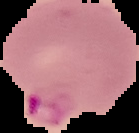

Summary:
  - Malaria status: parasitized
  - Preparation: thin blood smear
  - Image size: 139×133 pixels
  - Image type: cell region segmented out of the field of view; surrounding area masked to black